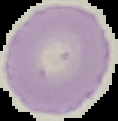

image size = 118×121 pixels
preparation = thin blood smear
image type = segmented cell region with the area outside set to black
malaria status = uninfected